Report the malaria status of this cell.
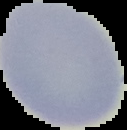

It is uninfected.

image size = 127×130 pixels
preparation = thin blood smear
image type = segmented cell region with the area outside set to black